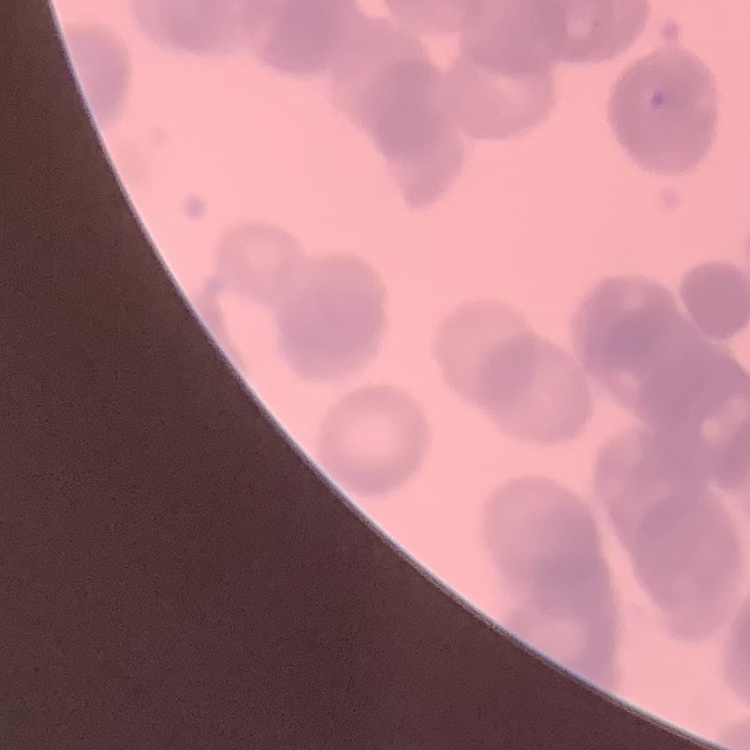
The erythrocytes show rouleaux formation. One tile cut from a larger photomicrograph. Thin blood smear. Stained with either Field's or Giemsa.